State which parasite is depicted.
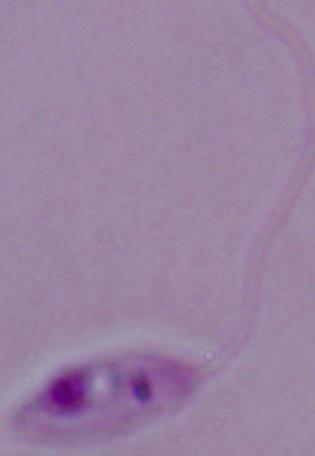
This is Leishmania.

1000x magnification. Micrograph.